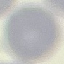
Malaria status: uninfected. Giemsa-stained preparation. Cell patch, automatically extracted from a larger field of view and resized to 64 × 64 pixels. Thin smear of blood. Acquired by smartphone through the microscope eyepiece.